Report the malaria status of this cell.
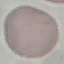

Uninfected.

capture = smartphone through the microscope eyepiece
image type = automatically extracted cell patch, resized to 64 × 64 pixels
stain = Giemsa
preparation = thin blood film